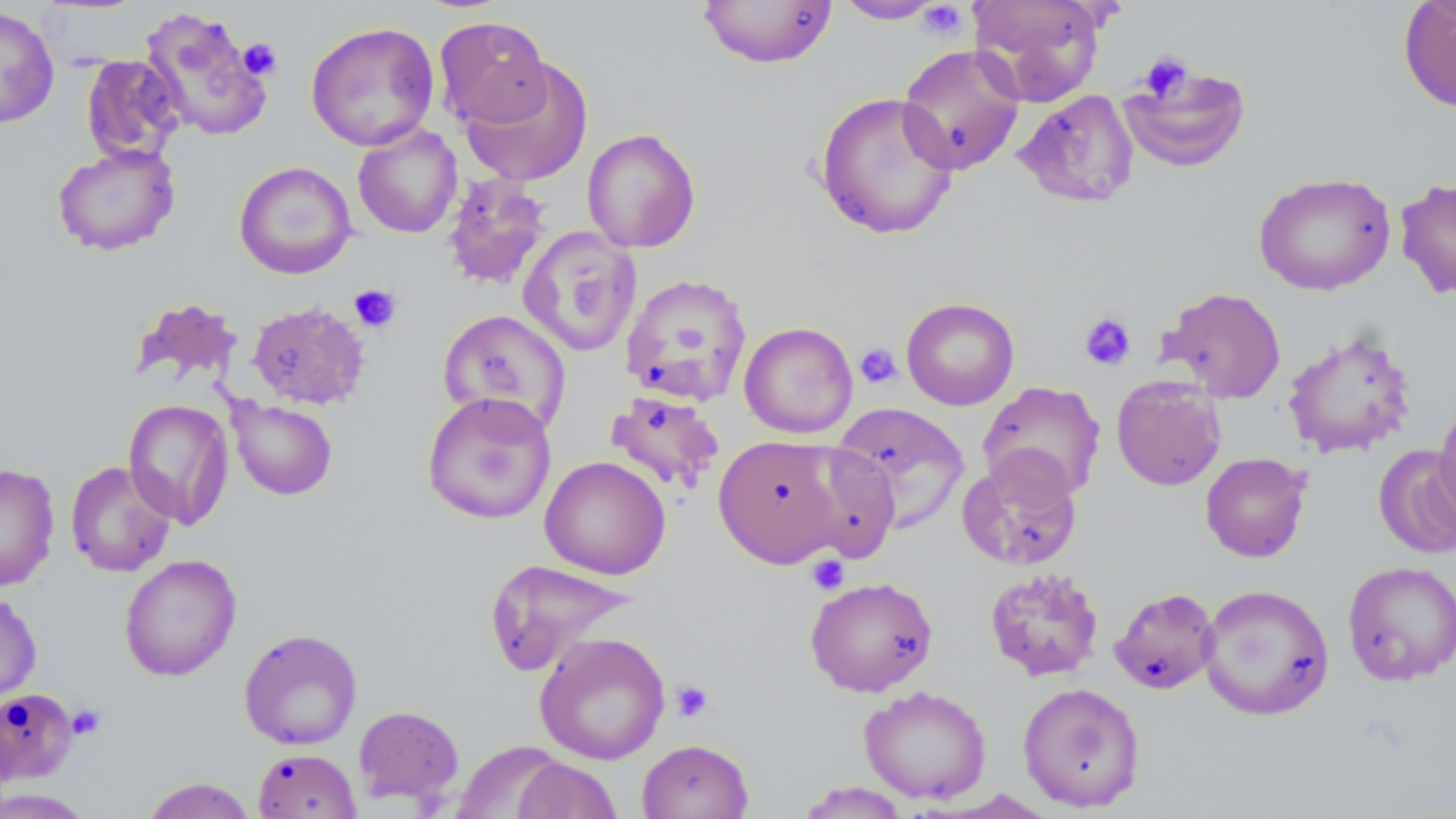

slide-level diagnosis = negative for blood parasites
magnification = 1000x
field of view = single
uninfected red blood cell locations = approximate bounding boxes as [x1, y1, x2, y2] in pixels: [697, 0, 837, 69], [833, 0, 947, 24], [970, 0, 1106, 106], [1398, 1, 1456, 113], [0, 5, 59, 128], [140, 6, 274, 141], [434, 16, 552, 130], [305, 21, 440, 151], [896, 44, 1025, 175], [80, 54, 184, 164], [460, 58, 595, 188], [1119, 63, 1252, 172], [1014, 89, 1139, 208], [814, 91, 960, 240], [352, 124, 463, 238], [582, 128, 701, 253], [52, 142, 180, 256], [234, 161, 357, 279], [441, 172, 553, 290], [1253, 172, 1396, 296], [1395, 177, 1456, 299], [517, 226, 642, 357], [620, 273, 752, 406], [1158, 286, 1287, 403], [130, 297, 242, 387], [901, 297, 1020, 410], [246, 300, 370, 410], [437, 309, 572, 436], [739, 321, 858, 438], [1283, 329, 1417, 458], [1111, 375, 1226, 491], [977, 380, 1106, 502], [604, 390, 725, 495], [422, 391, 557, 525], [123, 398, 235, 529], [228, 398, 337, 500], [1433, 400, 1456, 529], [830, 402, 970, 534], [713, 433, 849, 568], [789, 441, 901, 563], [1373, 444, 1456, 559], [956, 452, 1083, 571], [1200, 452, 1312, 563], [540, 456, 671, 579], [65, 461, 177, 578], [0, 463, 60, 591], [119, 554, 241, 681], [483, 558, 635, 676], [1342, 560, 1456, 687], [984, 567, 1104, 681], [804, 576, 939, 697], [1198, 583, 1335, 721], [1109, 587, 1220, 694], [0, 592, 42, 706], [239, 628, 363, 750], [534, 632, 671, 765], [1017, 682, 1146, 812], [859, 685, 992, 803], [0, 688, 78, 785], [353, 705, 464, 807], [637, 738, 754, 819], [454, 740, 568, 819], [253, 748, 361, 818], [512, 757, 622, 819], [140, 777, 256, 819], [796, 781, 911, 818], [0, 788, 94, 818]
preparation = thin blood film
platelet locations = approximate bounding boxes as [x1, y1, x2, y2] in pixels: [917, 1, 968, 40], [237, 38, 281, 79], [1139, 51, 1193, 103], [349, 284, 401, 333], [1079, 311, 1136, 371], [854, 342, 902, 389], [806, 554, 850, 596], [670, 680, 714, 723], [66, 704, 105, 740]
modality = light microscopy
image size = 1456×819 pixels
stain = May-Grünwald-Giemsa